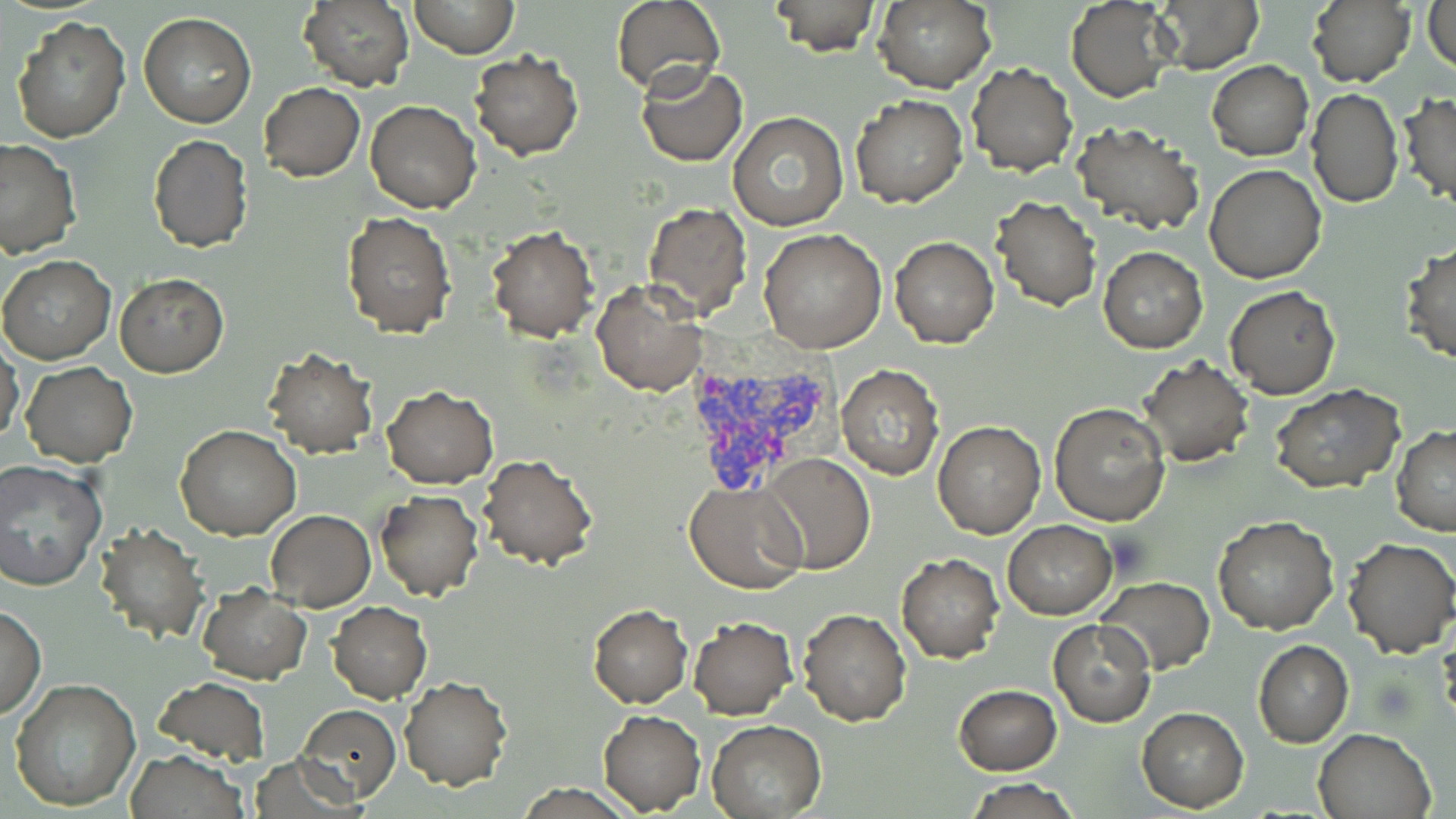

Summary:
  - Coordinate format: approximate bounding boxes as named x1/y1/x2/y2 corners in pixels
  - Plasmodium vivax-infected red blood cell locations: (x1=680, y1=359, x2=839, y2=496)
  - Uninfected red blood cell locations: (x1=297, y1=0, x2=416, y2=93), (x1=408, y1=0, x2=518, y2=59), (x1=611, y1=0, x2=724, y2=95), (x1=768, y1=0, x2=880, y2=54), (x1=1067, y1=0, x2=1178, y2=102), (x1=1154, y1=0, x2=1262, y2=72), (x1=1306, y1=0, x2=1415, y2=89), (x1=872, y1=1, x2=996, y2=93), (x1=1425, y1=1, x2=1456, y2=74), (x1=139, y1=13, x2=255, y2=129), (x1=9, y1=14, x2=131, y2=141), (x1=469, y1=51, x2=585, y2=160), (x1=1207, y1=60, x2=1313, y2=161), (x1=966, y1=61, x2=1077, y2=177), (x1=636, y1=63, x2=746, y2=167), (x1=259, y1=82, x2=365, y2=182), (x1=1307, y1=89, x2=1403, y2=208), (x1=1399, y1=93, x2=1456, y2=206), (x1=848, y1=94, x2=966, y2=208), (x1=366, y1=100, x2=480, y2=213), (x1=728, y1=111, x2=848, y2=231), (x1=1072, y1=121, x2=1204, y2=235), (x1=148, y1=135, x2=253, y2=252), (x1=0, y1=138, x2=80, y2=259), (x1=1205, y1=163, x2=1327, y2=283), (x1=991, y1=195, x2=1100, y2=311), (x1=641, y1=200, x2=752, y2=320), (x1=342, y1=210, x2=455, y2=337), (x1=485, y1=226, x2=598, y2=342), (x1=759, y1=228, x2=888, y2=354), (x1=889, y1=238, x2=999, y2=348), (x1=1401, y1=243, x2=1456, y2=366), (x1=1098, y1=246, x2=1207, y2=353), (x1=0, y1=255, x2=117, y2=365), (x1=115, y1=274, x2=228, y2=377), (x1=592, y1=279, x2=707, y2=396), (x1=1225, y1=286, x2=1341, y2=399), (x1=0, y1=344, x2=24, y2=445), (x1=263, y1=348, x2=378, y2=458), (x1=1138, y1=358, x2=1253, y2=468), (x1=21, y1=363, x2=137, y2=467), (x1=836, y1=364, x2=944, y2=480), (x1=1271, y1=385, x2=1404, y2=495), (x1=383, y1=387, x2=497, y2=489), (x1=1050, y1=402, x2=1171, y2=526), (x1=932, y1=419, x2=1046, y2=538), (x1=175, y1=424, x2=301, y2=540), (x1=1391, y1=426, x2=1456, y2=536), (x1=760, y1=452, x2=876, y2=574), (x1=479, y1=454, x2=598, y2=571), (x1=0, y1=458, x2=107, y2=594), (x1=685, y1=481, x2=809, y2=594), (x1=375, y1=491, x2=484, y2=601), (x1=266, y1=510, x2=376, y2=611), (x1=1212, y1=515, x2=1339, y2=635), (x1=1004, y1=519, x2=1117, y2=618), (x1=95, y1=523, x2=209, y2=644), (x1=1341, y1=537, x2=1456, y2=657), (x1=896, y1=552, x2=1004, y2=661), (x1=1097, y1=576, x2=1215, y2=675), (x1=197, y1=583, x2=311, y2=683), (x1=326, y1=601, x2=433, y2=703), (x1=0, y1=604, x2=45, y2=721), (x1=588, y1=605, x2=693, y2=710), (x1=798, y1=609, x2=910, y2=726), (x1=688, y1=616, x2=797, y2=719), (x1=1049, y1=620, x2=1156, y2=728), (x1=1253, y1=641, x2=1353, y2=747), (x1=155, y1=676, x2=269, y2=767), (x1=9, y1=677, x2=140, y2=812), (x1=398, y1=677, x2=512, y2=792), (x1=953, y1=684, x2=1061, y2=775), (x1=296, y1=704, x2=401, y2=804), (x1=1137, y1=708, x2=1249, y2=812), (x1=599, y1=711, x2=705, y2=814), (x1=706, y1=720, x2=827, y2=817), (x1=1313, y1=727, x2=1437, y2=819), (x1=124, y1=749, x2=249, y2=818), (x1=964, y1=778, x2=1081, y2=818)
  - Slide-level diagnosis: Plasmodium vivax
  - Field of view: single
  - Preparation: thin blood smear
  - Image size: 1456×819 pixels
  - Magnification: 1000x
  - Stain: May-Grünwald-Giemsa
  - Modality: optical microscopy